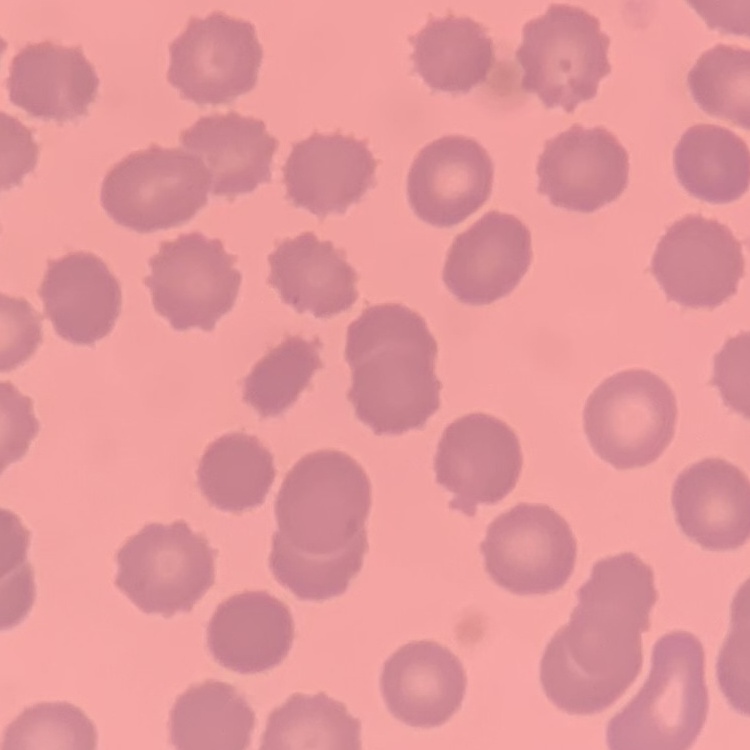

The red blood cells show no rouleaux formation. Stained with either Field's or Giemsa. Thin blood film. One tile cut from a larger photomicrograph.